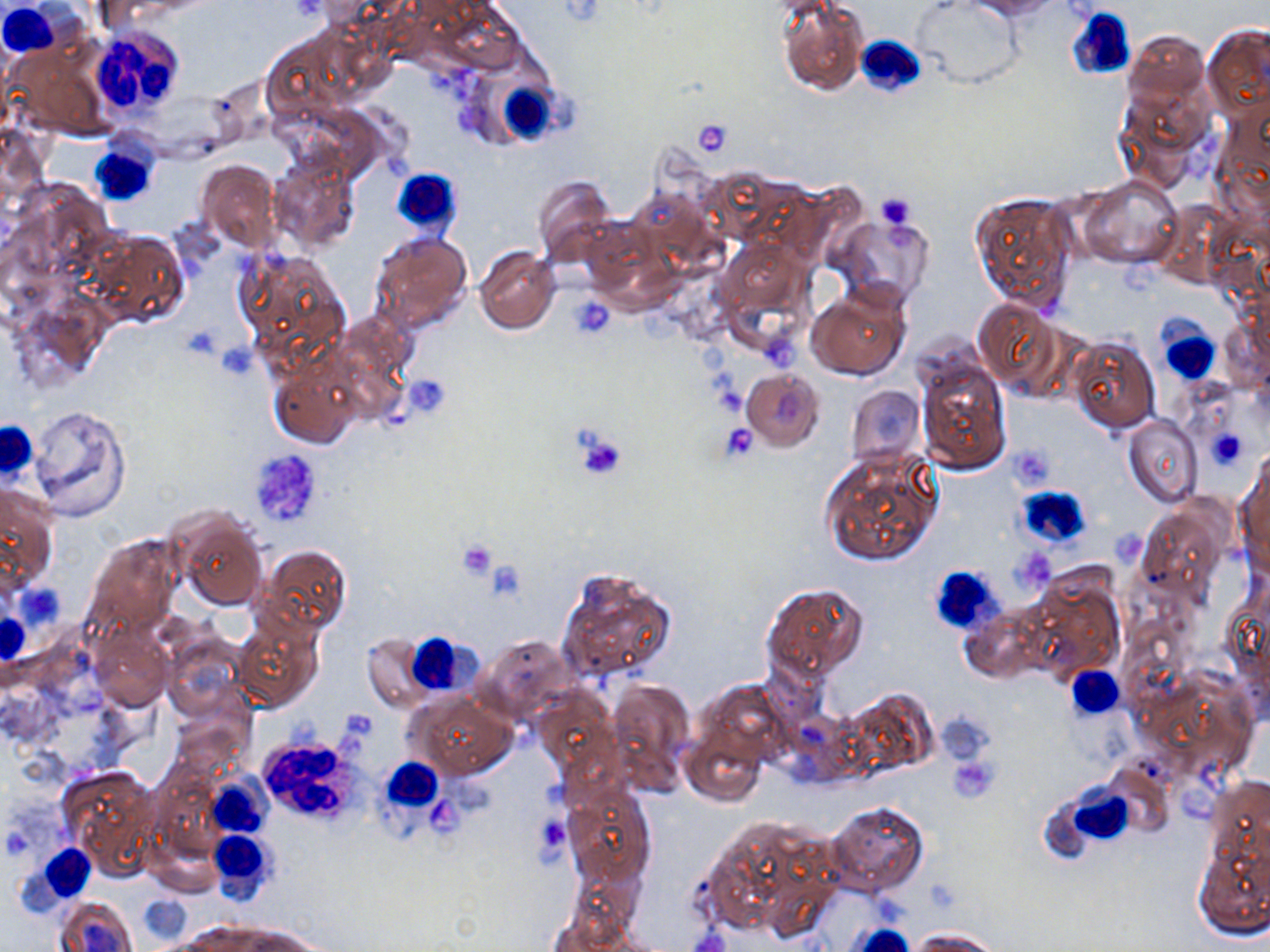

Summary:
  - Coordinate format: approximate bounding boxes as [x1, y1, x2, y2] in pixels
  - White blood cell locations: [1, 3, 67, 53], [1066, 7, 1136, 84], [87, 27, 189, 112], [855, 36, 925, 97], [502, 74, 575, 145], [93, 136, 166, 204], [391, 169, 464, 230], [1157, 310, 1218, 388], [0, 420, 40, 482], [1018, 485, 1093, 548], [927, 564, 1007, 637], [0, 609, 30, 664], [405, 632, 472, 695], [1070, 666, 1125, 720], [254, 731, 366, 826], [375, 762, 477, 834], [203, 769, 272, 841], [1066, 788, 1136, 844], [206, 829, 277, 904], [33, 844, 96, 905]
  - Platelet locations: [288, 0, 325, 22], [691, 120, 732, 158], [874, 191, 918, 231], [571, 297, 613, 337], [214, 340, 260, 379], [403, 374, 451, 416], [720, 423, 761, 463], [1207, 427, 1246, 471], [574, 430, 627, 482], [246, 447, 324, 530], [1010, 447, 1058, 484], [457, 540, 498, 580], [1016, 551, 1058, 597], [484, 561, 525, 603], [16, 582, 65, 630], [948, 756, 999, 801], [532, 812, 573, 865], [137, 895, 190, 943]
  - Uninfected red blood cell locations: [778, 0, 866, 95], [969, 0, 1059, 18], [915, 1, 1019, 87], [1204, 24, 1270, 121], [1124, 29, 1209, 110], [1115, 90, 1208, 191], [270, 154, 359, 253], [197, 160, 282, 253], [1078, 175, 1183, 269], [533, 176, 615, 264], [969, 190, 1078, 313], [832, 213, 933, 305], [84, 229, 188, 327], [369, 232, 472, 334], [716, 241, 811, 346], [235, 246, 351, 366], [475, 247, 560, 334], [807, 283, 911, 380], [973, 297, 1066, 396], [1069, 334, 1160, 433], [916, 357, 1012, 473], [270, 363, 361, 449], [740, 368, 825, 451], [844, 384, 926, 470], [26, 406, 131, 520], [1124, 418, 1202, 506], [818, 447, 942, 568], [1236, 460, 1269, 569], [1, 483, 59, 593], [1133, 503, 1230, 615], [172, 510, 269, 612], [85, 533, 180, 637], [257, 544, 351, 637], [553, 567, 677, 688], [1018, 573, 1124, 686], [762, 581, 869, 687], [232, 612, 324, 713], [92, 628, 171, 711], [161, 633, 248, 723], [359, 633, 440, 713], [473, 634, 573, 722], [606, 677, 694, 794], [698, 680, 793, 771], [532, 688, 620, 783], [844, 688, 939, 777], [409, 693, 518, 780], [170, 707, 249, 778], [682, 728, 767, 806], [59, 766, 160, 872], [1207, 776, 1269, 869], [562, 786, 655, 888], [825, 801, 928, 898], [699, 814, 840, 940], [1197, 843, 1269, 936], [55, 895, 136, 952], [181, 923, 261, 950], [245, 927, 321, 952], [912, 928, 1003, 952]
  - Slide-level diagnosis: no evidence of blood parasites
  - Stain: May-Grünwald-Giemsa
  - Preparation: thin blood film
  - Image size: 1270×952 pixels
  - Field of view: one of a larger specimen
  - Modality: light microscopy
  - Magnification: 1000x